Assess this cell for malaria.
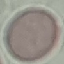
It is uninfected.

Summary:
  - Capture: smartphone camera at the microscope eyepiece
  - Preparation: thin smear
  - Image type: automatically extracted cell patch, resized to 64 × 64 pixels
  - Stain: Giemsa